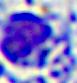

Summary:
  - Identification: leukocyte
  - Magnification: 400x
  - Modality: photomicrograph